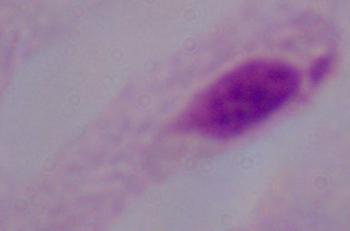 A trichomonad is seen. Photomicrograph. 1000x magnification.